Locate every blood parasite and identify its species.
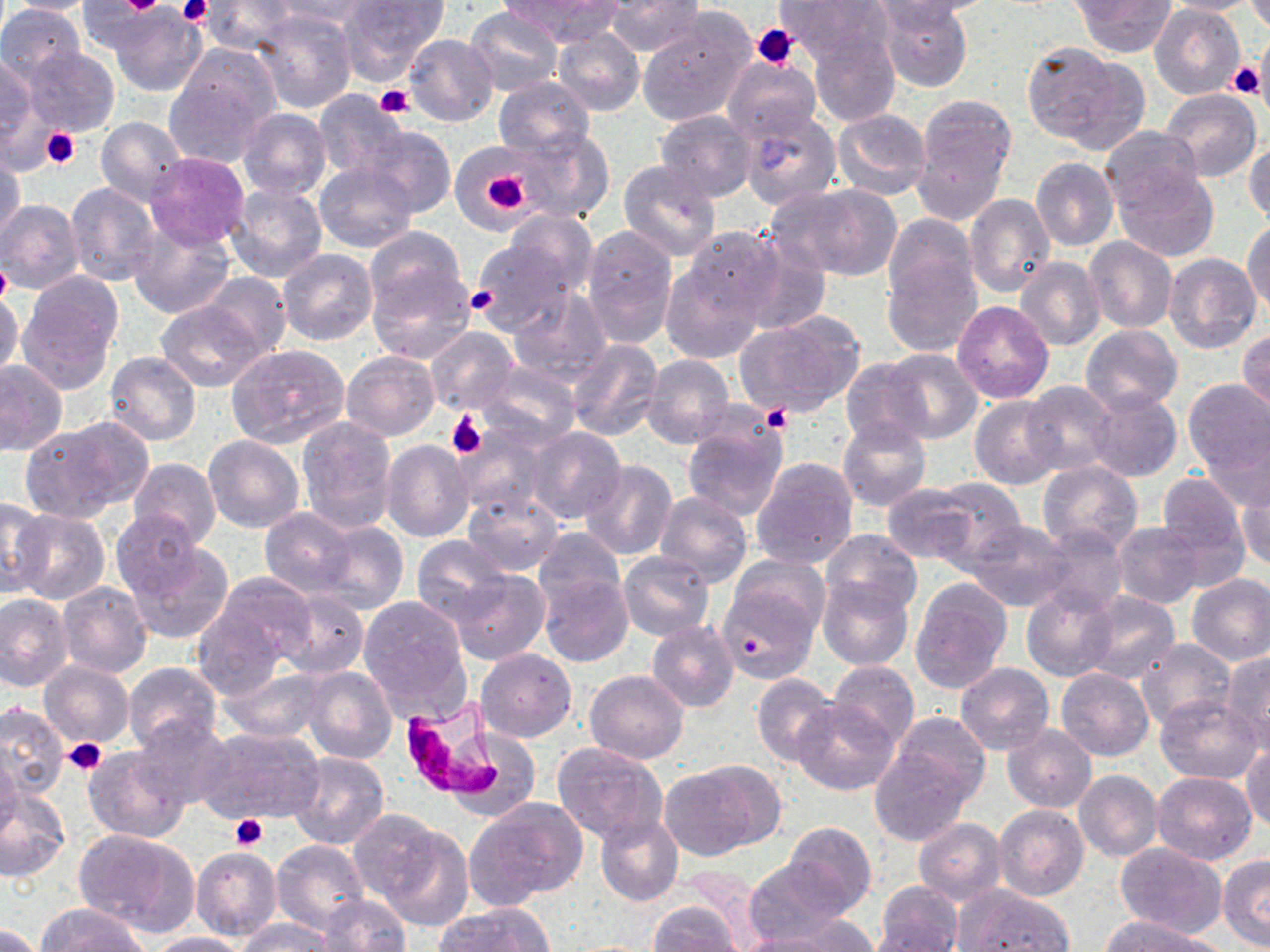

Approximate bounding boxes as (x1, y1, x2, y2) in pixels.
Plasmodium falciparum-infected red blood cells: (398, 703, 496, 793).
No Plasmodium ovale, Plasmodium malariae, Plasmodium vivax, Babesia divergens, or Trypanosoma brucei observed.

Platelet locations: (118, 0, 165, 14), (177, 0, 212, 26), (751, 23, 801, 69), (1230, 64, 1263, 100), (375, 84, 414, 118), (41, 128, 80, 168), (474, 162, 533, 220), (0, 258, 11, 307), (465, 285, 498, 315), (761, 405, 792, 433), (447, 410, 486, 459), (65, 738, 107, 775), (231, 815, 267, 851). Uninfected red blood cell locations: (2, 0, 103, 14), (202, 0, 294, 55), (510, 0, 616, 42), (605, 0, 704, 56), (775, 0, 891, 66), (877, 0, 972, 92), (884, 0, 1005, 18), (1071, 0, 1177, 57), (1159, 0, 1266, 14), (78, 1, 160, 55), (269, 1, 375, 32), (340, 1, 449, 81), (1246, 1, 1269, 35), (1150, 4, 1246, 101), (0, 6, 84, 85), (466, 6, 563, 96), (108, 7, 206, 97), (254, 8, 357, 113), (636, 15, 754, 126), (553, 27, 644, 117), (808, 30, 901, 128), (404, 33, 498, 127), (1022, 43, 1141, 151), (23, 47, 118, 136), (166, 47, 278, 162), (0, 53, 40, 153), (724, 56, 822, 144), (494, 76, 595, 162), (314, 87, 408, 180), (1159, 87, 1261, 183), (913, 95, 1017, 210), (237, 108, 330, 201), (735, 108, 843, 211), (654, 109, 757, 201), (833, 109, 930, 199), (96, 117, 187, 204), (514, 125, 617, 223), (357, 126, 457, 218), (1099, 126, 1203, 219), (1245, 135, 1270, 225), (455, 145, 536, 229), (144, 151, 250, 250), (0, 153, 24, 247), (1031, 156, 1118, 251), (617, 160, 722, 261), (315, 163, 416, 252), (1113, 165, 1220, 262), (66, 183, 159, 286), (225, 183, 328, 282), (779, 184, 903, 281), (964, 194, 1054, 297), (0, 199, 85, 294), (503, 210, 598, 296), (883, 213, 977, 304), (128, 216, 235, 319), (1244, 218, 1270, 317), (580, 224, 678, 348), (362, 226, 468, 320), (682, 226, 785, 321), (735, 232, 831, 339), (1084, 236, 1177, 333), (470, 240, 577, 338), (278, 249, 377, 345), (881, 253, 981, 356), (1164, 254, 1261, 355), (659, 258, 767, 365), (1015, 258, 1105, 352), (366, 265, 477, 364), (200, 271, 291, 360), (17, 275, 122, 390), (508, 287, 610, 386), (0, 289, 22, 382), (155, 299, 269, 392), (953, 301, 1054, 403), (737, 313, 864, 417), (1081, 324, 1183, 414), (425, 327, 518, 415), (1239, 329, 1269, 417), (565, 339, 663, 442), (228, 344, 350, 448), (881, 348, 984, 443), (341, 349, 438, 440), (105, 353, 202, 445), (641, 354, 734, 448), (841, 358, 931, 449), (0, 359, 66, 456), (478, 361, 579, 449), (1181, 380, 1270, 479), (1021, 381, 1118, 477), (1084, 387, 1183, 483), (970, 394, 1063, 491), (682, 412, 788, 520), (296, 416, 397, 532), (837, 418, 931, 512), (18, 423, 135, 523), (527, 427, 626, 524), (454, 428, 549, 516), (1203, 431, 1270, 512), (203, 435, 304, 533), (381, 439, 473, 543), (1224, 442, 1270, 551), (129, 457, 221, 549), (752, 457, 859, 568), (579, 461, 678, 563), (1036, 462, 1143, 557), (1238, 471, 1270, 571), (1156, 473, 1252, 582), (925, 479, 1025, 565), (880, 483, 979, 566), (462, 487, 564, 576), (655, 491, 753, 588), (0, 498, 50, 595), (260, 508, 357, 597), (12, 510, 111, 605), (111, 510, 203, 601), (962, 518, 1077, 613), (314, 520, 407, 615), (1112, 521, 1207, 609), (1035, 526, 1132, 615), (532, 527, 626, 610), (821, 528, 923, 616), (413, 535, 514, 627), (128, 541, 235, 643), (617, 551, 715, 641), (727, 554, 829, 640), (449, 568, 549, 665), (537, 571, 633, 667), (205, 572, 318, 668), (1185, 573, 1270, 666), (818, 576, 912, 670), (909, 576, 1012, 696), (58, 580, 153, 678), (717, 581, 821, 684), (1022, 585, 1117, 682), (1079, 590, 1180, 685), (275, 592, 367, 678), (0, 595, 73, 692), (358, 595, 471, 712), (190, 607, 287, 700), (647, 620, 739, 712), (1134, 639, 1235, 731), (476, 648, 576, 742), (1221, 652, 1270, 752), (829, 659, 918, 751), (39, 661, 134, 748), (122, 662, 220, 753), (955, 662, 1054, 756), (219, 666, 329, 744), (301, 666, 397, 764), (1055, 667, 1154, 761), (585, 670, 688, 764), (751, 671, 841, 767), (1154, 696, 1263, 784), (791, 698, 899, 796), (0, 702, 68, 798), (888, 711, 992, 809), (134, 718, 235, 812), (1002, 724, 1098, 812), (197, 726, 324, 825), (551, 740, 668, 841), (870, 743, 975, 847), (1242, 743, 1270, 831), (0, 745, 22, 840), (83, 746, 191, 844), (288, 751, 389, 850), (663, 759, 780, 858), (1074, 771, 1163, 860), (1150, 772, 1256, 865), (0, 785, 70, 882), (469, 798, 588, 905), (993, 804, 1089, 902), (363, 815, 473, 924), (595, 815, 683, 907), (914, 817, 1005, 905), (782, 821, 877, 915), (73, 828, 200, 936), (270, 839, 369, 933), (1114, 842, 1225, 937), (190, 847, 283, 940), (1218, 855, 1270, 950), (742, 860, 851, 945), (873, 882, 964, 952), (953, 885, 1073, 952), (314, 895, 411, 951), (646, 902, 745, 952), (436, 903, 554, 952), (36, 904, 152, 952), (779, 915, 879, 952), (1102, 915, 1219, 952), (235, 917, 333, 951), (864, 923, 963, 950), (0, 924, 48, 952), (142, 932, 252, 952), (732, 932, 842, 952). Slide-level diagnosis: Plasmodium falciparum. One field of a larger specimen. Captured at 1000x magnification. May-Grünwald-Giemsa-stained preparation. Thin blood film. Image is 1270×952 pixels. Light microscopy.